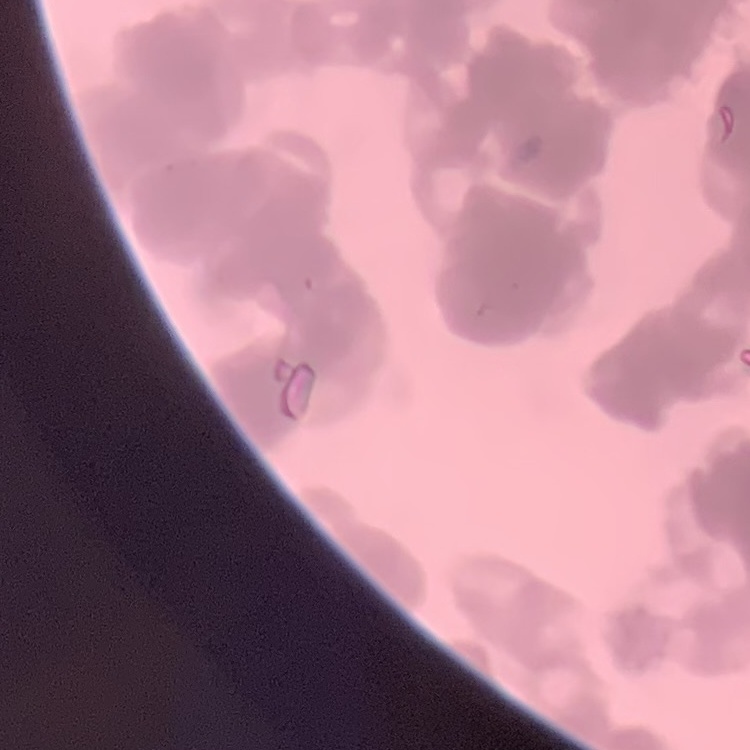 The red blood cells show rouleaux formation. Thin peripheral smear. Stained with either Field's or Giemsa. One tile cut from a larger photomicrograph.